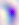

magnification: 400x
modality: micrograph
identification: Toxoplasma gondii